Outline each Plasmodium falciparum-infected red blood cell.
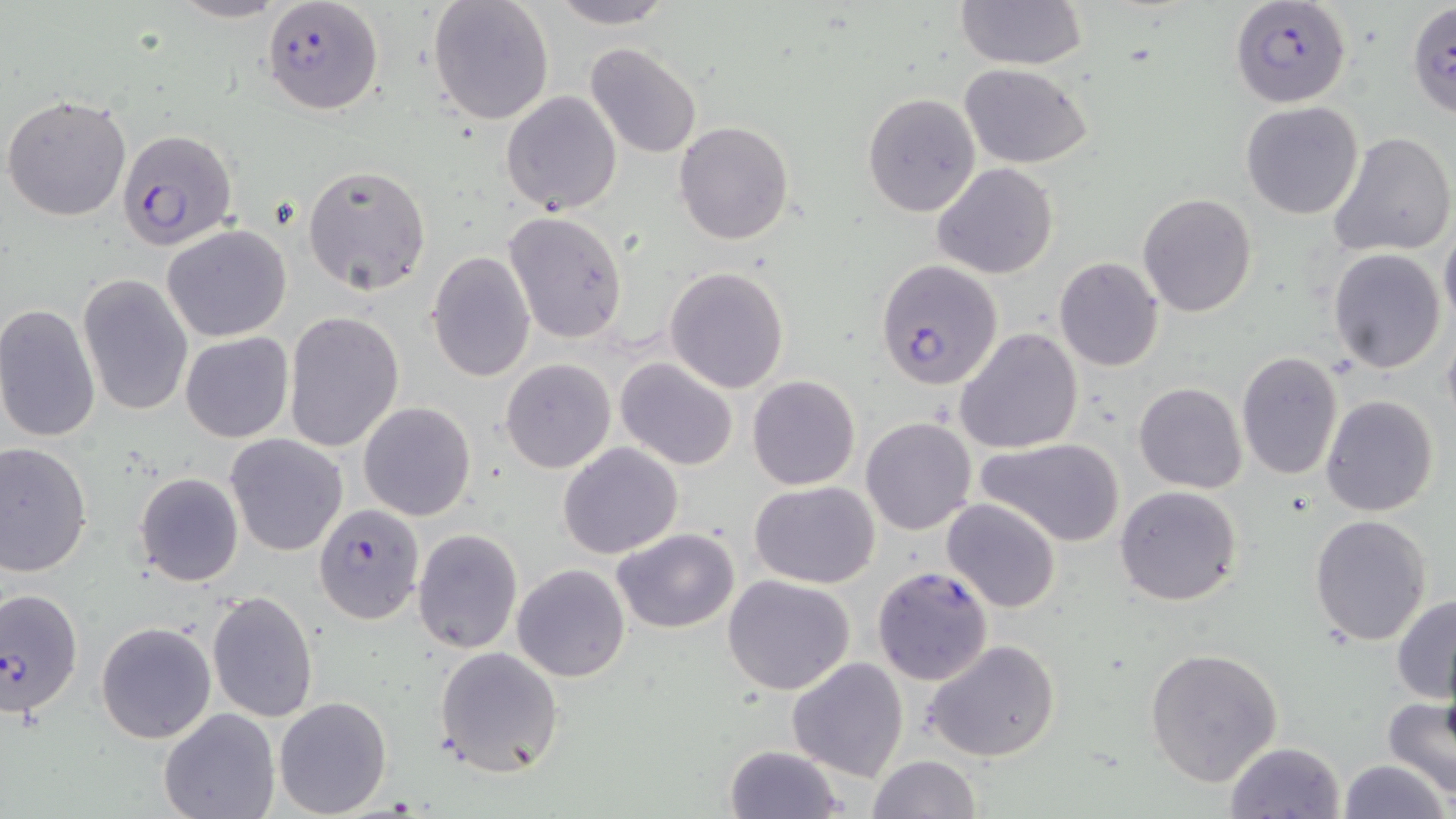
Approximate bounding boxes as [x1, y1, x2, y2] in pixels.
Plasmodium falciparum-infected red blood cells: [262, 0, 383, 116], [1232, 0, 1350, 108], [116, 128, 238, 253], [875, 258, 1004, 390], [313, 504, 424, 624], [871, 565, 992, 682], [1, 584, 85, 718].

slide-level diagnosis = Plasmodium falciparum
preparation = thin blood film
uninfected red blood cell locations = approximate bounding boxes as [x1, y1, x2, y2] in pixels: [167, 0, 290, 24], [428, 0, 555, 126], [545, 0, 678, 28], [955, 0, 1088, 70], [1406, 4, 1455, 116], [584, 42, 702, 160], [960, 64, 1093, 167], [500, 90, 622, 215], [861, 92, 982, 218], [2, 93, 132, 222], [1242, 102, 1364, 220], [674, 121, 796, 244], [1328, 131, 1456, 258], [302, 163, 431, 295], [932, 163, 1058, 279], [1137, 191, 1257, 318], [503, 210, 628, 344], [1439, 222, 1456, 333], [161, 225, 292, 343], [1327, 248, 1447, 373], [426, 251, 536, 381], [1054, 257, 1165, 372], [664, 266, 790, 394], [77, 274, 193, 416], [0, 303, 101, 444], [282, 311, 404, 453], [1440, 322, 1456, 433], [954, 327, 1085, 455], [180, 331, 294, 442], [1235, 350, 1342, 481], [501, 358, 614, 473], [615, 358, 739, 470], [748, 375, 860, 490], [1133, 381, 1247, 495], [1321, 395, 1438, 516], [359, 401, 476, 521], [861, 416, 976, 534], [224, 433, 348, 556], [977, 438, 1124, 548], [0, 441, 93, 577], [558, 442, 683, 559], [133, 471, 244, 587], [750, 481, 880, 586], [1115, 485, 1241, 606], [942, 498, 1061, 612], [1309, 513, 1432, 647], [412, 527, 523, 655], [613, 528, 741, 634], [513, 565, 631, 682], [723, 575, 857, 694], [207, 591, 318, 723], [1392, 593, 1456, 703], [95, 621, 216, 743], [922, 640, 1063, 764], [433, 646, 563, 776], [1145, 646, 1283, 786], [786, 656, 909, 779], [273, 695, 392, 817], [1384, 697, 1456, 801], [159, 708, 279, 819], [1223, 741, 1346, 819], [725, 745, 846, 819], [867, 754, 981, 819], [1337, 758, 1450, 819]
image size = 1456×819 pixels
stain = May-Grünwald-Giemsa
field of view = single
magnification = 1000x
modality = light microscopy